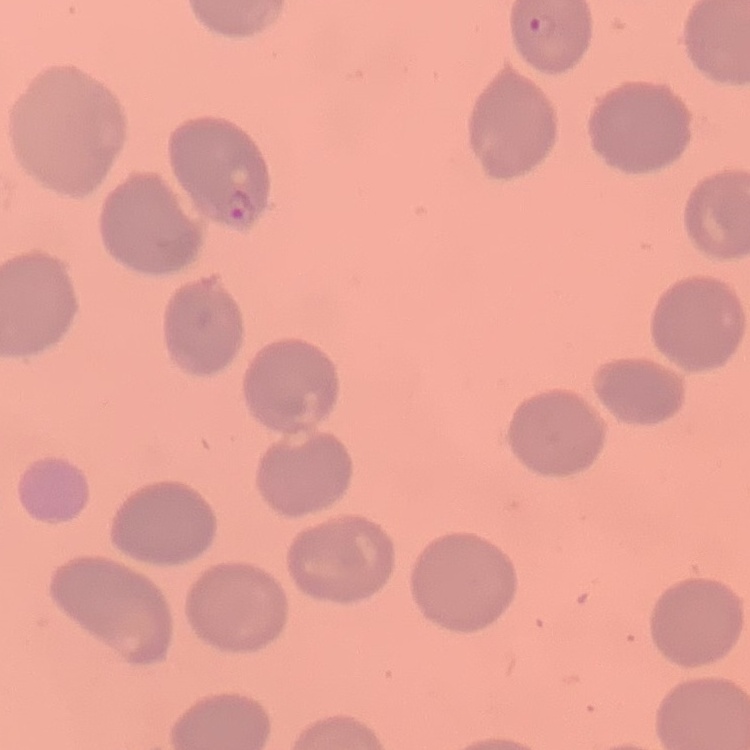

The red blood cells exhibit no rouleaux formation. Thin blood smear. Stained with either Field's or Giemsa. Square crop of a larger photomicrograph.